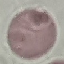
Summary:
  - Malaria status: uninfected
  - Image type: automatically extracted cell patch, resized to 64 × 64 pixels
  - Capture: smartphone camera at the microscope eyepiece
  - Stain: Giemsa
  - Preparation: thin smear